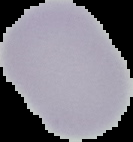 Image is 133×142 pixels. From a thin blood smear. Malaria status: uninfected. The area outside the segmented cell region is set to black.